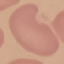 Malaria status: uninfected. Photographed with a smartphone camera at the microscope eyepiece. Giemsa-stained preparation. Thin smear of blood. Cell patch, automatically extracted from a larger field of view and resized to 64 × 64 pixels.